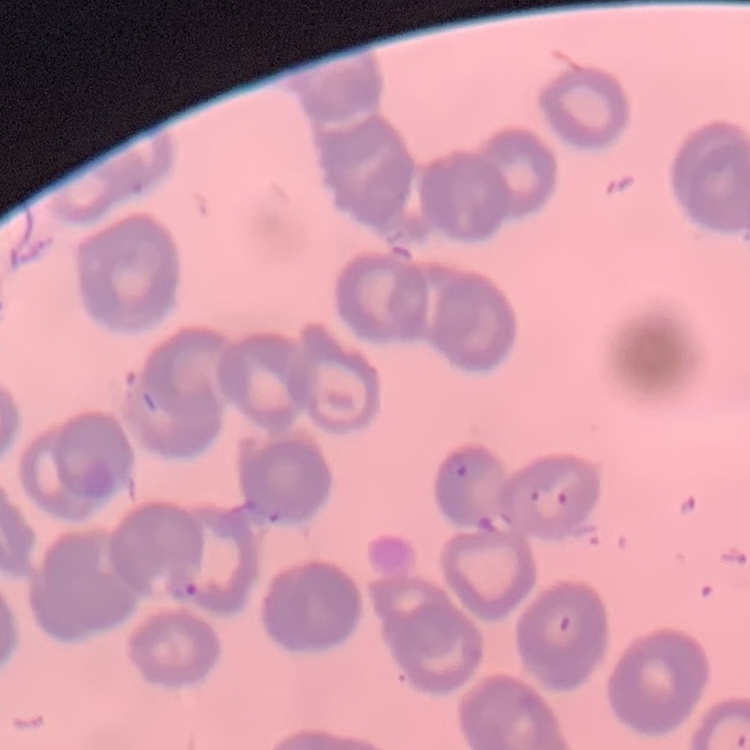 The red blood cells show rouleaux formation. Stained with either Field's or Giemsa. Square crop of a larger photomicrograph. Thin peripheral smear.